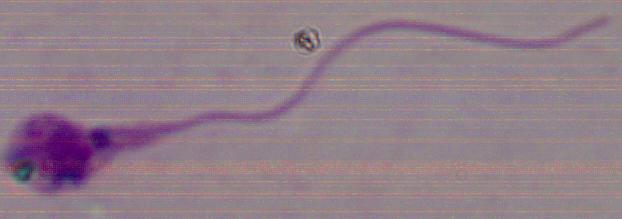

identification = Leishmania
magnification = 1000x
modality = micrograph